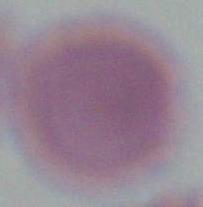 An erythrocyte is shown. 1000x magnification. Micrograph.